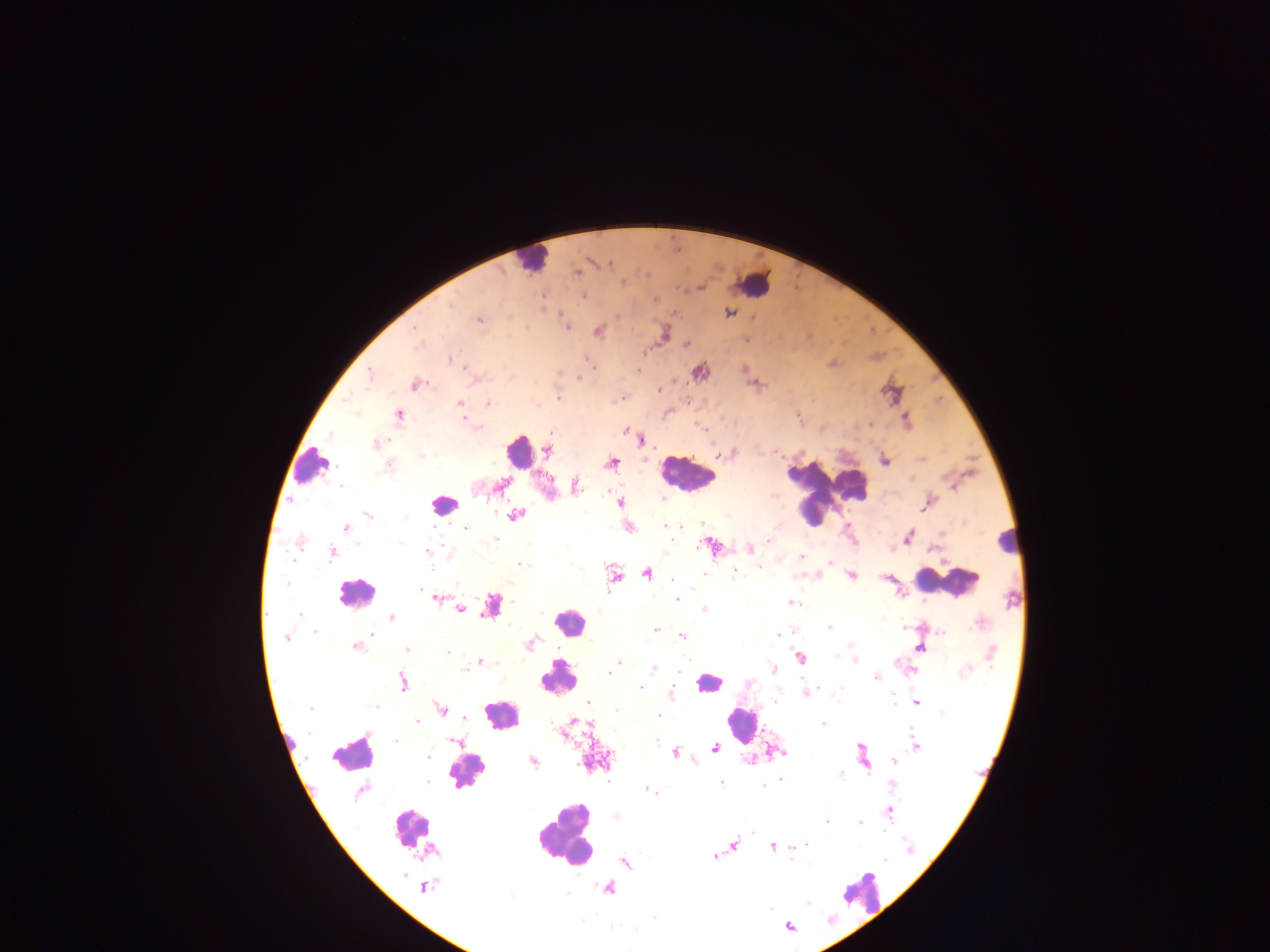

Approximate centers as (x, y) in pixels. Leukocyte locations: (531, 259), (752, 284), (519, 451), (311, 465), (686, 472), (827, 493), (443, 502), (1007, 541), (947, 582), (355, 593), (491, 604), (568, 623), (558, 677), (708, 682), (502, 714), (740, 723), (352, 753), (466, 772), (409, 828), (565, 832), (861, 891). Plasmodium parasite locations: (607, 263), (575, 271), (583, 295), (542, 298), (727, 312), (478, 320), (566, 327), (414, 330), (598, 331), (664, 333), (747, 340), (416, 344), (687, 344), (449, 358), (464, 367), (743, 369), (700, 371), (370, 372), (415, 384), (757, 384), (658, 390), (558, 397), (622, 397), (459, 404), (488, 404), (398, 415), (797, 416), (905, 420), (625, 430), (639, 440), (377, 444), (547, 449), (723, 453), (729, 453), (884, 460), (611, 462), (389, 464), (501, 485), (574, 487), (619, 503), (928, 503), (516, 514), (367, 515), (666, 526), (345, 527), (628, 527), (463, 529), (907, 536), (769, 542), (711, 545), (750, 549), (425, 551), (331, 553), (800, 557), (830, 561), (520, 564), (734, 571), (647, 572), (613, 575), (703, 575), (814, 575), (851, 575), (886, 578), (435, 597), (677, 598), (790, 603), (459, 608), (703, 609), (300, 616), (391, 617), (980, 622), (829, 627), (654, 629), (942, 631), (315, 632), (682, 636), (286, 638), (355, 645), (529, 645), (407, 647), (920, 647), (448, 653), (799, 656), (854, 661), (480, 662), (619, 662), (615, 665), (654, 668), (613, 669), (773, 669), (464, 670), (910, 670), (608, 672), (876, 677), (402, 681), (750, 683), (640, 687), (671, 693), (804, 693), (588, 701), (917, 702), (312, 708), (440, 709), (463, 717), (417, 721), (822, 724), (565, 730), (395, 740), (457, 741), (915, 745), (715, 748), (773, 751), (675, 752), (427, 755), (863, 756), (533, 760), (894, 760), (839, 773), (780, 781), (721, 783), (892, 784), (649, 789), (362, 790), (888, 812), (616, 816), (826, 820), (860, 821), (733, 845), (772, 846), (804, 846), (715, 856), (884, 860), (624, 861), (425, 887), (608, 887), (788, 925). Collected in Ghana. Mobile-phone photograph taken through the microscope. Image is 1270×952 pixels. Thick blood film. Single field of view.